Name the blood parasite species.
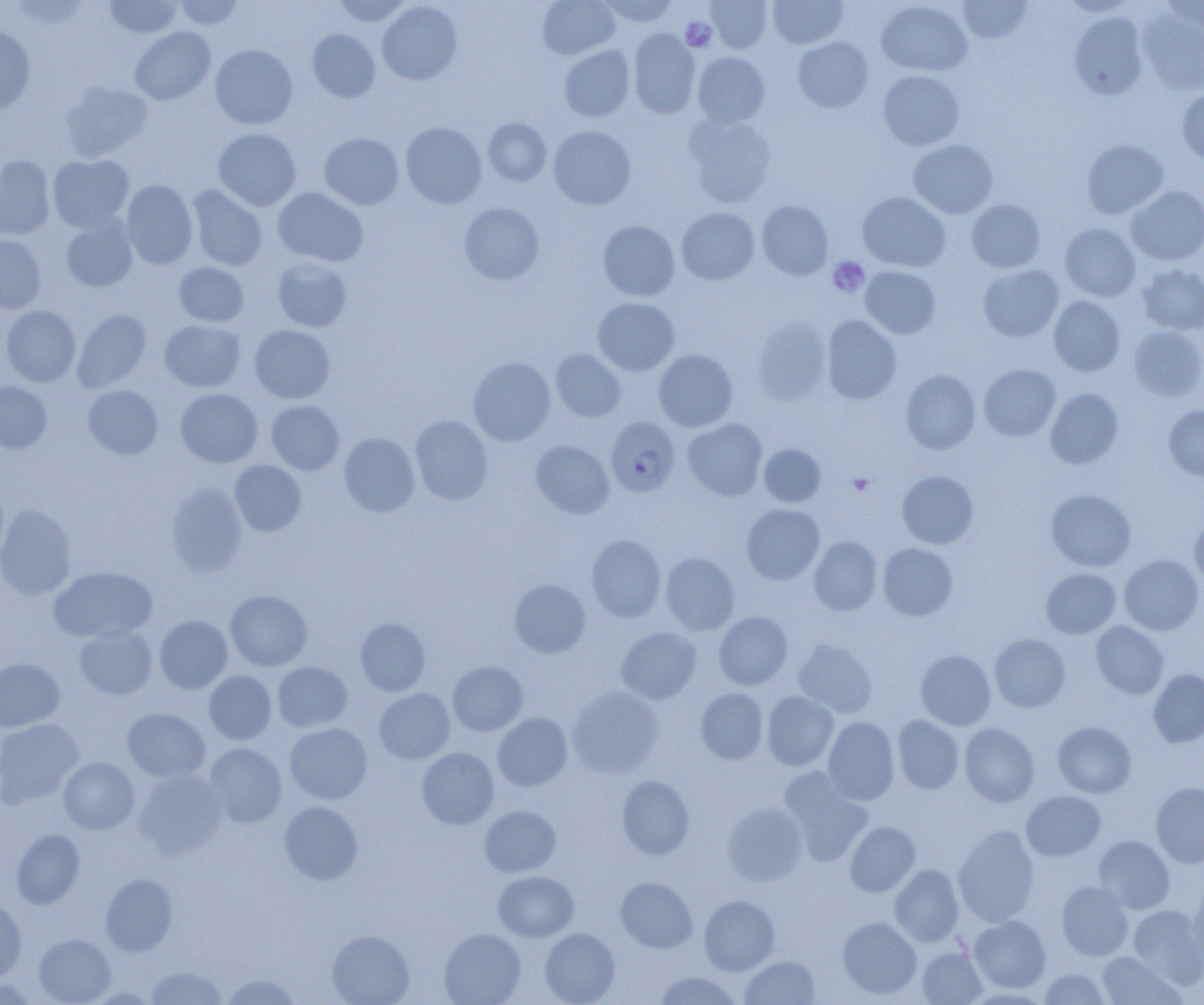

Plasmodium falciparum.

Summary:
  - Coordinate format: approximate bounding boxes as named x1/y1/x2/y2 corners in pixels
  - Uninfected red blood cell locations: (x1=104, y1=0, x2=183, y2=39), (x1=174, y1=0, x2=244, y2=29), (x1=537, y1=0, x2=620, y2=59), (x1=597, y1=0, x2=677, y2=28), (x1=705, y1=0, x2=773, y2=53), (x1=768, y1=0, x2=848, y2=49), (x1=957, y1=0, x2=1032, y2=44), (x1=1057, y1=0, x2=1140, y2=17), (x1=332, y1=1, x2=413, y2=27), (x1=377, y1=1, x2=462, y2=85), (x1=876, y1=1, x2=973, y2=76), (x1=1160, y1=1, x2=1204, y2=37), (x1=1138, y1=9, x2=1204, y2=96), (x1=1070, y1=12, x2=1148, y2=99), (x1=130, y1=26, x2=215, y2=105), (x1=0, y1=27, x2=36, y2=115), (x1=628, y1=28, x2=700, y2=119), (x1=307, y1=29, x2=380, y2=103), (x1=793, y1=37, x2=873, y2=113), (x1=210, y1=44, x2=297, y2=130), (x1=559, y1=45, x2=635, y2=122), (x1=692, y1=52, x2=769, y2=128), (x1=878, y1=70, x2=964, y2=150), (x1=59, y1=81, x2=153, y2=162), (x1=1177, y1=86, x2=1204, y2=163), (x1=684, y1=114, x2=777, y2=207), (x1=483, y1=118, x2=551, y2=186), (x1=401, y1=122, x2=487, y2=208), (x1=548, y1=125, x2=636, y2=210), (x1=213, y1=128, x2=300, y2=211), (x1=319, y1=132, x2=404, y2=210), (x1=908, y1=139, x2=998, y2=218), (x1=1081, y1=139, x2=1169, y2=219), (x1=48, y1=155, x2=134, y2=233), (x1=0, y1=156, x2=56, y2=240), (x1=121, y1=180, x2=198, y2=269), (x1=187, y1=184, x2=267, y2=271), (x1=1126, y1=186, x2=1204, y2=265), (x1=272, y1=187, x2=369, y2=267), (x1=858, y1=192, x2=951, y2=272), (x1=966, y1=199, x2=1045, y2=273), (x1=757, y1=200, x2=833, y2=280), (x1=459, y1=202, x2=544, y2=284), (x1=677, y1=207, x2=759, y2=284), (x1=61, y1=216, x2=138, y2=292), (x1=597, y1=220, x2=680, y2=301), (x1=1060, y1=223, x2=1141, y2=302), (x1=0, y1=235, x2=45, y2=313), (x1=272, y1=257, x2=352, y2=332), (x1=174, y1=262, x2=249, y2=327), (x1=978, y1=264, x2=1064, y2=342), (x1=1137, y1=264, x2=1204, y2=335), (x1=860, y1=266, x2=940, y2=338), (x1=1048, y1=296, x2=1125, y2=376), (x1=593, y1=297, x2=680, y2=375), (x1=1, y1=305, x2=81, y2=387), (x1=72, y1=309, x2=151, y2=392), (x1=822, y1=315, x2=901, y2=404), (x1=751, y1=317, x2=831, y2=405), (x1=159, y1=320, x2=245, y2=392), (x1=250, y1=325, x2=335, y2=403), (x1=1128, y1=326, x2=1204, y2=401), (x1=550, y1=349, x2=625, y2=422), (x1=654, y1=349, x2=737, y2=431), (x1=468, y1=357, x2=555, y2=446), (x1=979, y1=364, x2=1060, y2=441), (x1=901, y1=370, x2=981, y2=454), (x1=0, y1=381, x2=52, y2=453), (x1=83, y1=385, x2=163, y2=459), (x1=175, y1=388, x2=262, y2=468), (x1=1045, y1=388, x2=1123, y2=469), (x1=266, y1=400, x2=344, y2=475), (x1=1164, y1=405, x2=1204, y2=481), (x1=410, y1=415, x2=492, y2=505), (x1=683, y1=419, x2=767, y2=501), (x1=339, y1=432, x2=420, y2=517), (x1=531, y1=440, x2=615, y2=519), (x1=758, y1=444, x2=825, y2=507), (x1=230, y1=460, x2=306, y2=536), (x1=897, y1=470, x2=978, y2=549), (x1=165, y1=481, x2=247, y2=576), (x1=1046, y1=489, x2=1136, y2=571), (x1=0, y1=504, x2=76, y2=600), (x1=742, y1=504, x2=824, y2=584), (x1=1189, y1=514, x2=1204, y2=590), (x1=586, y1=534, x2=666, y2=623), (x1=809, y1=536, x2=882, y2=615), (x1=877, y1=542, x2=958, y2=620), (x1=660, y1=552, x2=739, y2=634), (x1=1119, y1=555, x2=1203, y2=635), (x1=48, y1=566, x2=157, y2=642), (x1=1041, y1=568, x2=1120, y2=638), (x1=509, y1=579, x2=591, y2=657), (x1=225, y1=589, x2=312, y2=671), (x1=714, y1=611, x2=793, y2=690), (x1=154, y1=615, x2=233, y2=694), (x1=355, y1=617, x2=430, y2=696), (x1=1091, y1=621, x2=1169, y2=698), (x1=75, y1=625, x2=157, y2=699), (x1=616, y1=627, x2=701, y2=704), (x1=989, y1=633, x2=1071, y2=712), (x1=793, y1=638, x2=877, y2=717), (x1=915, y1=650, x2=996, y2=730), (x1=0, y1=658, x2=65, y2=732), (x1=272, y1=661, x2=352, y2=732), (x1=447, y1=661, x2=528, y2=736), (x1=1148, y1=669, x2=1204, y2=747), (x1=204, y1=671, x2=276, y2=745), (x1=567, y1=686, x2=663, y2=778), (x1=374, y1=688, x2=455, y2=763), (x1=695, y1=688, x2=767, y2=764), (x1=762, y1=691, x2=838, y2=771), (x1=122, y1=707, x2=210, y2=782), (x1=492, y1=713, x2=572, y2=791), (x1=892, y1=715, x2=965, y2=794), (x1=823, y1=716, x2=899, y2=805), (x1=0, y1=718, x2=83, y2=808), (x1=1053, y1=721, x2=1136, y2=797), (x1=284, y1=723, x2=372, y2=804), (x1=959, y1=723, x2=1039, y2=807), (x1=204, y1=742, x2=286, y2=827), (x1=416, y1=748, x2=498, y2=829), (x1=58, y1=757, x2=139, y2=834), (x1=778, y1=767, x2=873, y2=866), (x1=134, y1=769, x2=228, y2=858), (x1=617, y1=775, x2=694, y2=859), (x1=1151, y1=782, x2=1204, y2=868), (x1=1021, y1=791, x2=1105, y2=861), (x1=279, y1=801, x2=363, y2=884), (x1=722, y1=802, x2=808, y2=886), (x1=480, y1=805, x2=561, y2=877), (x1=845, y1=821, x2=920, y2=897), (x1=953, y1=825, x2=1040, y2=927), (x1=11, y1=829, x2=85, y2=909), (x1=1094, y1=835, x2=1175, y2=914), (x1=889, y1=863, x2=964, y2=946), (x1=494, y1=870, x2=578, y2=941), (x1=100, y1=874, x2=177, y2=956), (x1=616, y1=877, x2=698, y2=953), (x1=1188, y1=880, x2=1204, y2=965), (x1=1056, y1=881, x2=1134, y2=960), (x1=699, y1=895, x2=780, y2=975), (x1=0, y1=898, x2=27, y2=982), (x1=1128, y1=904, x2=1203, y2=986), (x1=969, y1=916, x2=1050, y2=993), (x1=838, y1=917, x2=922, y2=999), (x1=439, y1=928, x2=526, y2=1005), (x1=540, y1=928, x2=620, y2=1005), (x1=326, y1=930, x2=414, y2=1005), (x1=34, y1=934, x2=115, y2=1005), (x1=917, y1=947, x2=986, y2=1004), (x1=1097, y1=951, x2=1183, y2=1004), (x1=740, y1=955, x2=820, y2=1004), (x1=146, y1=966, x2=226, y2=1004), (x1=1038, y1=968, x2=1110, y2=1004), (x1=654, y1=971, x2=743, y2=1004), (x1=221, y1=974, x2=301, y2=1004)
  - Platelet locations: (x1=681, y1=18, x2=717, y2=52), (x1=828, y1=257, x2=869, y2=297), (x1=849, y1=473, x2=874, y2=495)
  - Plasmodium falciparum-infected red blood cell locations: (x1=605, y1=416, x2=680, y2=497)
  - Preparation: thin blood smear
  - Image size: 1204×1005 pixels
  - Field of view: single
  - Magnification: 1000x
  - Modality: light microscopy